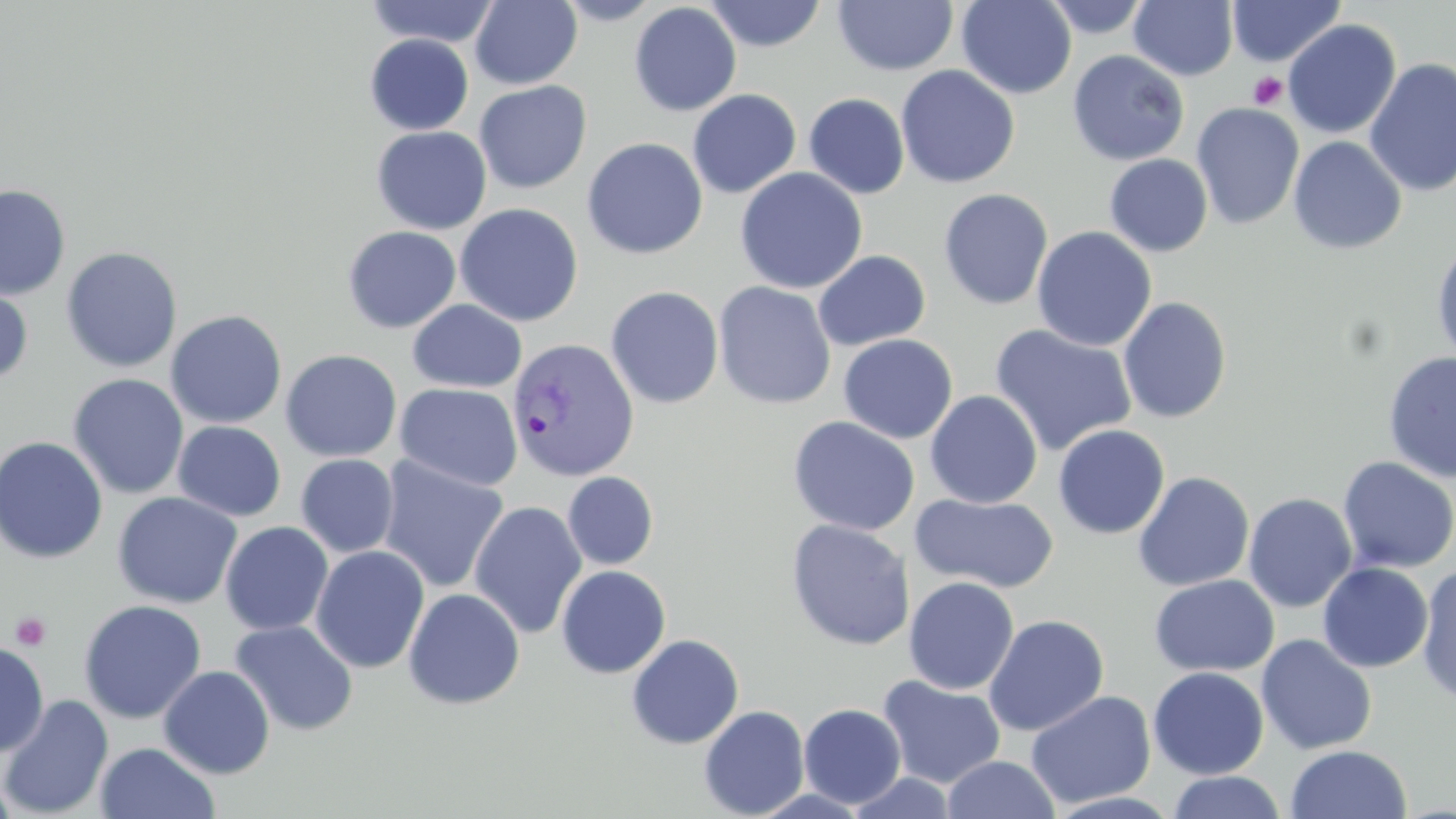

slide-level diagnosis = Plasmodium vivax
image size = 1456×819 pixels
platelet locations = approximate bounding boxes as (x1,y1)-(x2,y2) corner pairs in pixels: (1248,72)-(1288,111), (10,611)-(52,651)
uninfected red blood cell locations = approximate bounding boxes as (x1,y1)-(x2,y2) corner pairs in pixels: (469,0)-(582,89), (553,0)-(665,25), (956,0)-(1076,99), (1041,0)-(1151,39), (1227,0)-(1345,67), (363,1)-(500,48), (703,1)-(828,52), (832,1)-(958,76), (1129,1)-(1238,81), (629,2)-(742,116), (1282,19)-(1402,139), (364,34)-(474,135), (1067,49)-(1190,166), (1363,58)-(1456,197), (896,65)-(1020,189), (473,80)-(591,194), (687,89)-(801,198), (804,93)-(910,199), (1191,103)-(1305,230), (357,125)-(470,334), (371,126)-(492,234), (1287,135)-(1407,255), (582,137)-(708,259), (1104,153)-(1213,257), (734,167)-(868,294), (0,184)-(70,300), (938,188)-(1054,310), (455,203)-(583,326), (342,225)-(462,333), (1031,226)-(1157,352), (1431,239)-(1456,365), (60,246)-(183,373), (813,250)-(930,351), (0,279)-(34,388), (713,281)-(837,409), (605,286)-(724,409), (1118,296)-(1232,423), (407,299)-(527,393), (165,310)-(287,429), (989,324)-(1138,457), (838,334)-(958,443), (280,349)-(402,462), (1382,350)-(1456,483), (67,373)-(189,500), (396,383)-(523,491), (924,390)-(1043,508), (787,416)-(921,536), (173,421)-(286,521), (1053,424)-(1170,539), (0,436)-(108,564), (295,453)-(399,558), (377,455)-(509,594), (1337,456)-(1456,574), (562,471)-(659,569), (1133,471)-(1255,591), (112,492)-(243,609), (1243,492)-(1358,613), (910,493)-(1059,593), (468,501)-(587,639), (785,519)-(915,651), (220,521)-(334,636), (310,545)-(429,674), (1317,562)-(1434,673), (555,565)-(671,678), (1416,565)-(1456,706), (1148,573)-(1280,677), (903,576)-(1019,695), (403,587)-(525,709), (78,599)-(207,724), (983,614)-(1109,737), (229,619)-(358,736), (626,634)-(744,749), (1256,634)-(1378,755), (0,642)-(49,758), (158,665)-(275,779), (1148,666)-(1269,780), (877,675)-(1007,789), (1025,690)-(1157,809), (1,694)-(113,817), (799,703)-(907,809), (699,705)-(810,818), (94,741)-(221,819), (1285,744)-(1412,819), (942,754)-(1060,818), (1166,771)-(1287,819), (0,774)-(19,819)
field of view = one of a larger specimen
Plasmodium vivax-infected red blood cell locations = approximate bounding boxes as (x1,y1)-(x2,y2) corner pairs in pixels: (507,337)-(638,482)
modality = light microscopy
preparation = thin blood smear
magnification = 1000x
stain = May-Grünwald-Giemsa